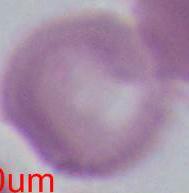

Summary:
  - Modality: micrograph
  - Identification: erythrocyte
  - Magnification: 1000x